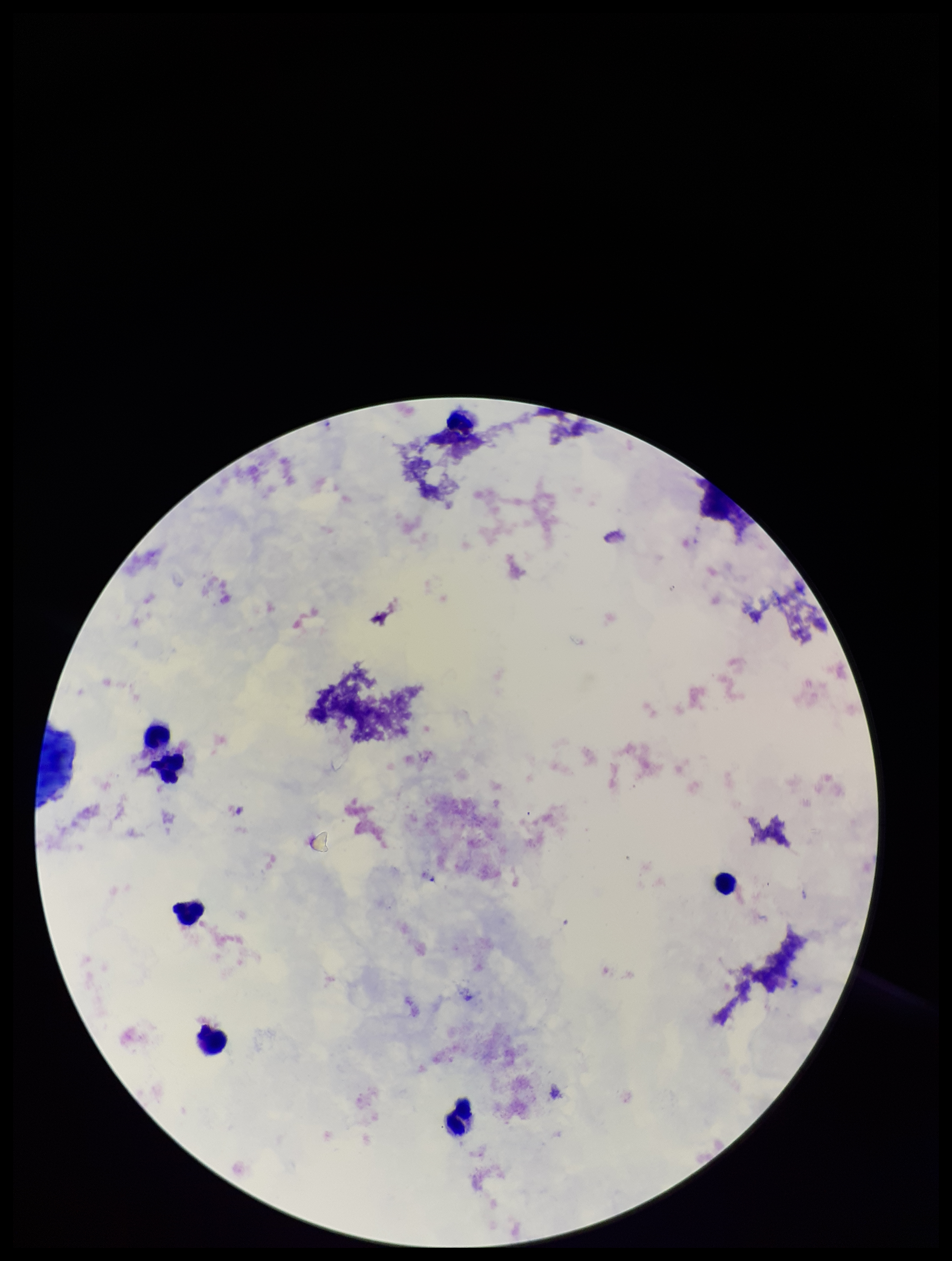 Giemsa stain. Smartphone photograph taken through the eyepiece of a microscope. Patient malaria status: negative. Image is 952×1261 pixels. Preparation: thick blood smear. Plasmodium parasites: none detected. Single field of view. Leukocyte count: 6. Parasite count: 0.